Look for Plasmodium parasites.
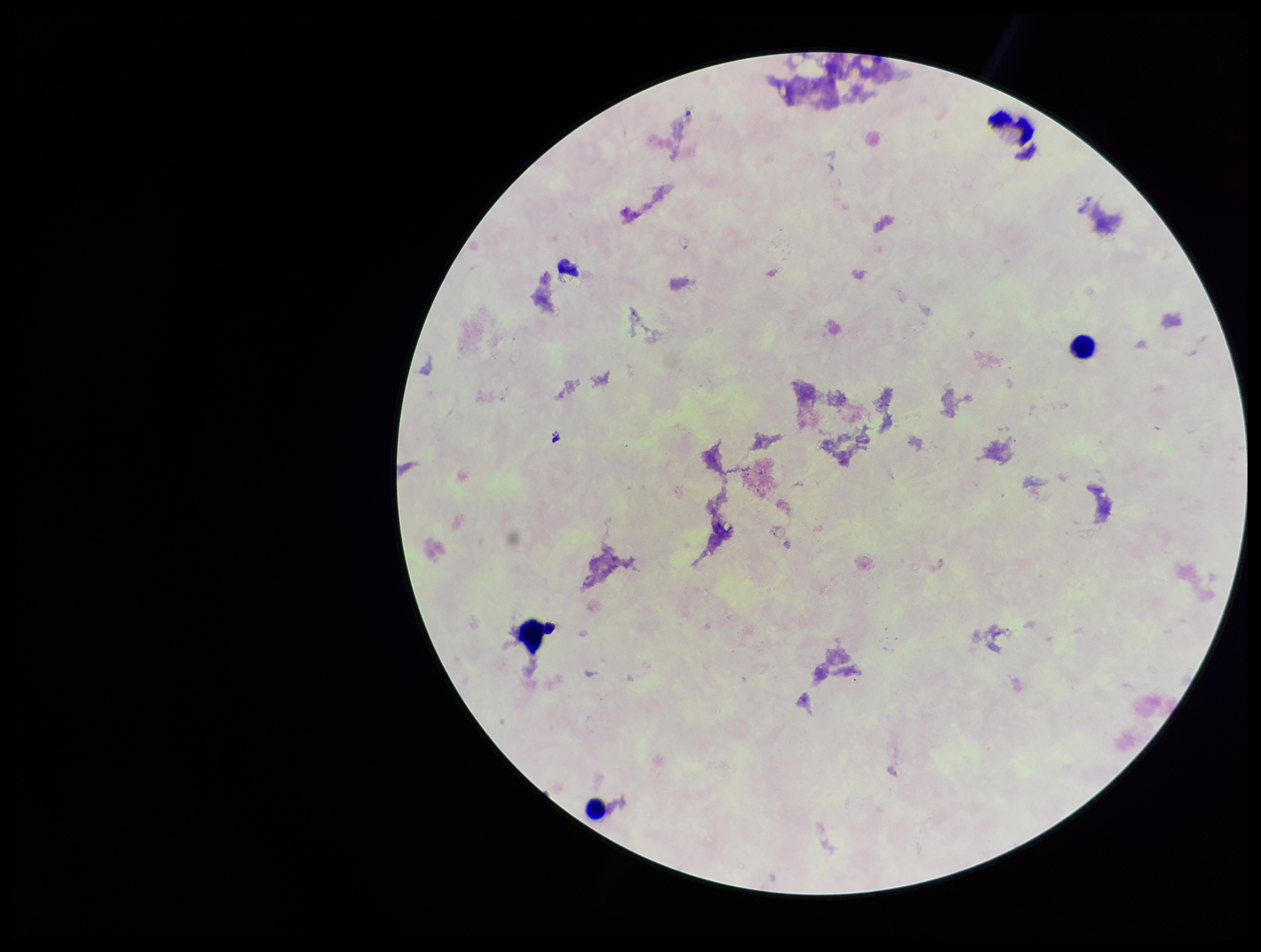

None detected.

One field from this slide. Image is 1261×952 pixels. Patient malaria status: negative. Giemsa stain. Leukocyte count: 3. Parasite count: 0. Photographed through the microscope eyepiece with a smartphone camera. Preparation: thick blood smear.